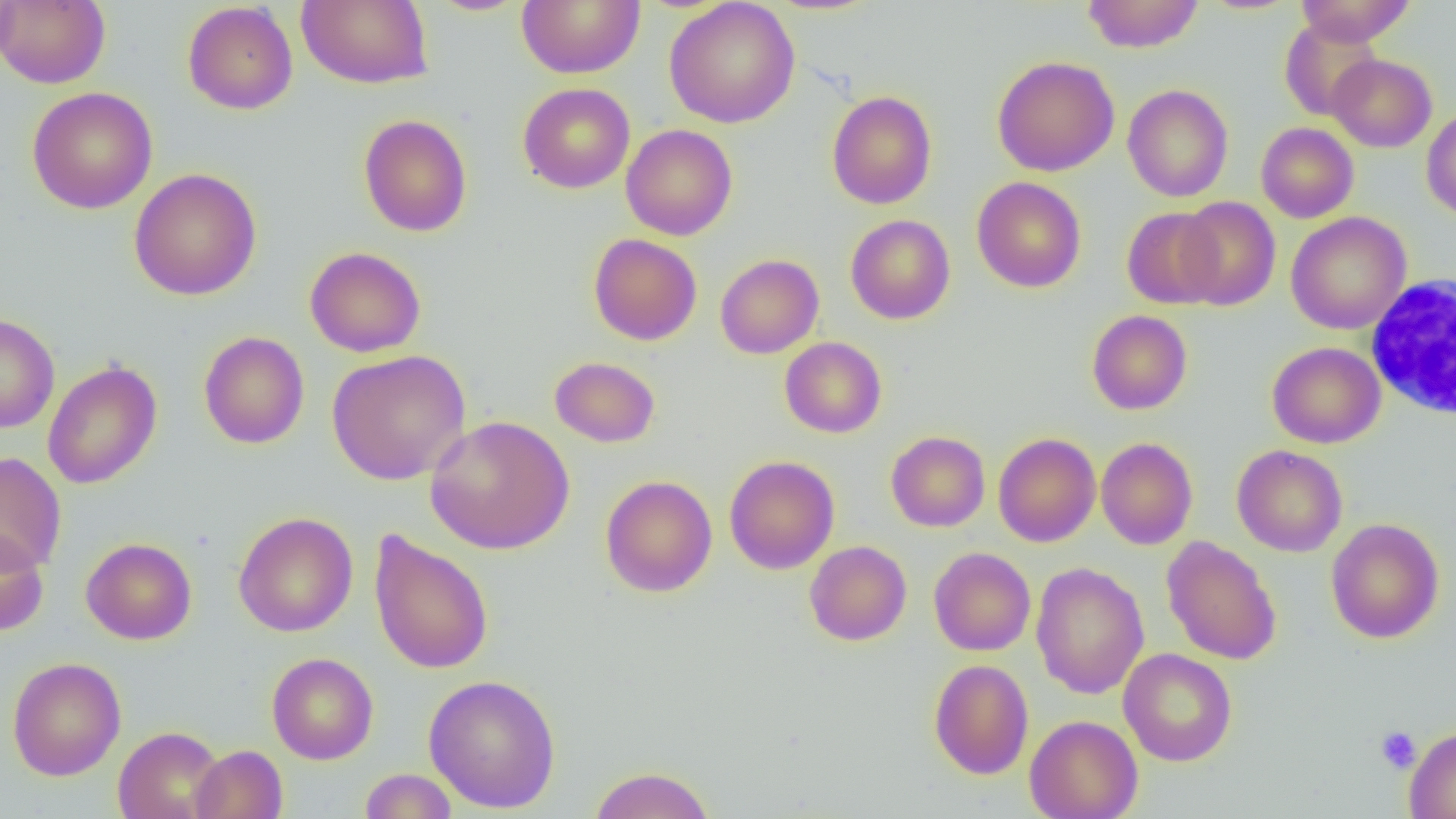

Approximate bounding boxes as (x1, y1, x2, y2) in pixels. White blood cell locations: (1364, 275, 1455, 421). Uninfected red blood cell locations: (0, 0, 19, 73), (1, 0, 111, 89), (296, 0, 434, 90), (517, 0, 645, 79), (663, 0, 800, 128), (1082, 0, 1204, 53), (1296, 0, 1417, 46), (426, 1, 530, 16), (182, 2, 298, 115), (1279, 18, 1383, 121), (1327, 54, 1437, 152), (992, 56, 1120, 177), (517, 83, 635, 193), (1122, 84, 1233, 202), (27, 86, 158, 214), (826, 90, 937, 209), (1421, 107, 1456, 221), (358, 114, 472, 237), (1256, 122, 1359, 223), (621, 123, 738, 241), (129, 168, 262, 300), (971, 176, 1086, 293), (1175, 196, 1281, 311), (1122, 206, 1225, 309), (1286, 212, 1412, 334), (845, 214, 955, 324), (588, 233, 702, 345), (304, 246, 426, 358), (715, 254, 824, 359), (1086, 310, 1193, 415), (0, 313, 59, 433), (198, 331, 310, 449), (779, 337, 887, 438), (1267, 342, 1386, 448), (326, 349, 471, 485), (550, 356, 661, 448), (43, 360, 162, 489), (425, 415, 575, 555), (886, 431, 990, 532), (993, 433, 1101, 547), (1096, 437, 1198, 550), (1232, 444, 1347, 557), (0, 452, 67, 573), (724, 455, 839, 574), (600, 475, 717, 597), (233, 511, 358, 637), (1325, 518, 1445, 644), (0, 528, 49, 636), (368, 529, 494, 675), (1161, 536, 1282, 665), (81, 537, 197, 645), (805, 541, 911, 646), (929, 547, 1036, 656), (1031, 562, 1149, 700), (1118, 648, 1237, 766), (267, 652, 378, 764), (7, 657, 126, 781), (929, 659, 1034, 780), (423, 673, 561, 813), (1024, 714, 1143, 819), (113, 726, 226, 819), (1404, 727, 1456, 818), (190, 745, 287, 819), (588, 766, 715, 819), (359, 768, 458, 818). Platelet locations: (1375, 726, 1421, 773). Slide-level diagnosis: no evidence of blood parasites. Thin blood film. Single field of view. Light microscopy. Captured at 1000x magnification. Image is 1456×819 pixels.